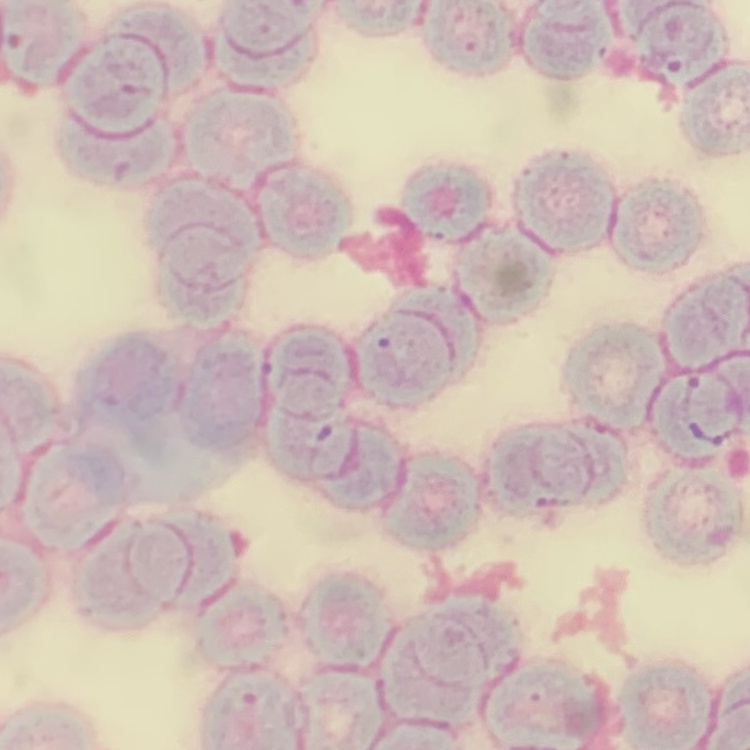 The red blood cells exhibit rouleaux formation. Stained with either Field's or Giemsa. Thin blood film. One tile cut from a larger photomicrograph.